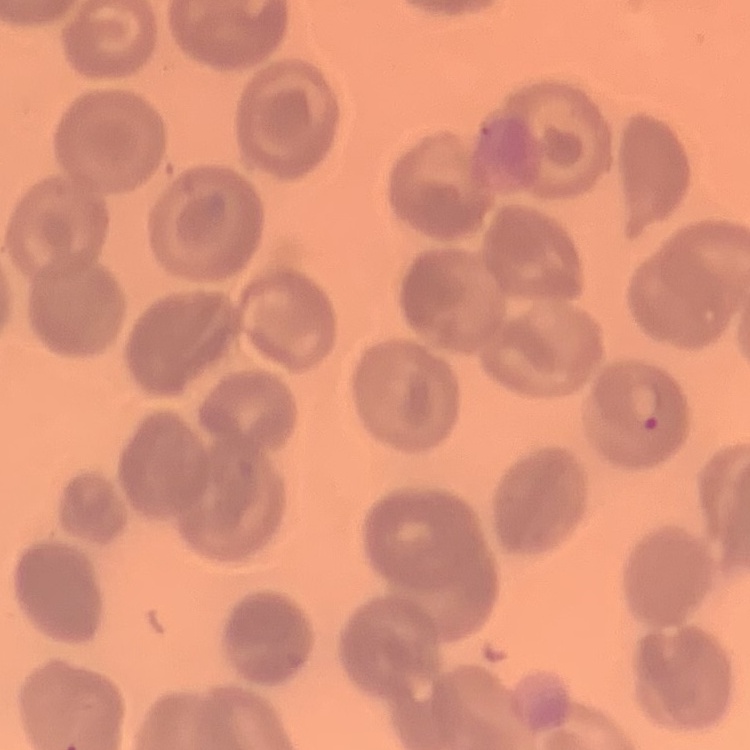

red blood cell morphology = no rouleaux formation
stain = Field's or Giemsa
image type = square crop of a larger photomicrograph
preparation = thin blood film